Describe the morphology of the red blood cells.
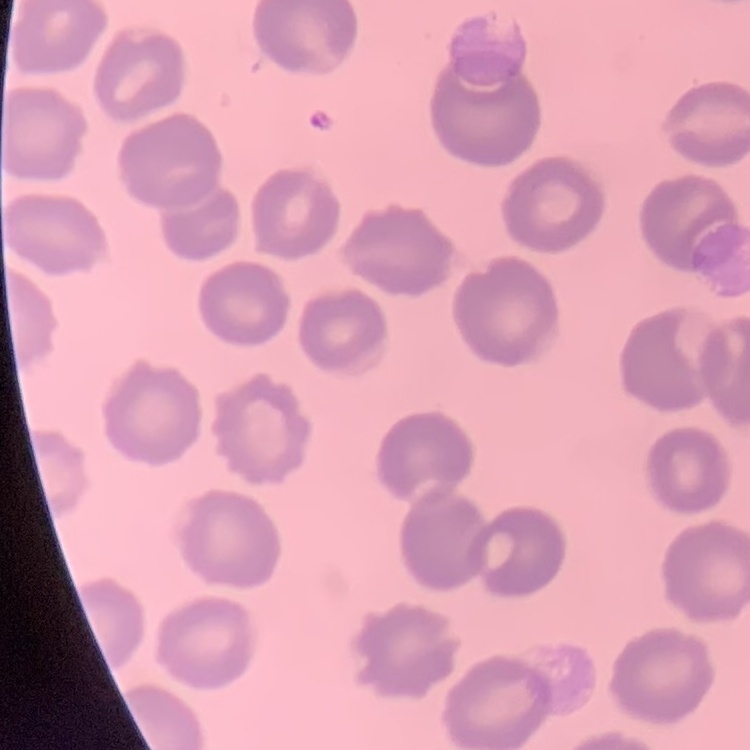

No rouleaux formation.

stain: Field's or Giemsa
preparation: thin peripheral smear
image_type: one tile cut from a larger photomicrograph